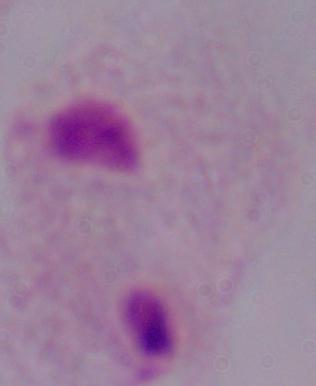
Summary:
  - Modality: photomicrograph
  - Magnification: 1000x
  - Identification: trichomonad